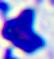
modality = photomicrograph
magnification = 400x
identification = white blood cell